Classify this cell by malaria status.
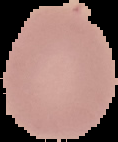

It is uninfected.

Summary:
  - Image size: 118×142 pixels
  - Image type: segmented cell region with the area outside set to black
  - Preparation: thin blood smear